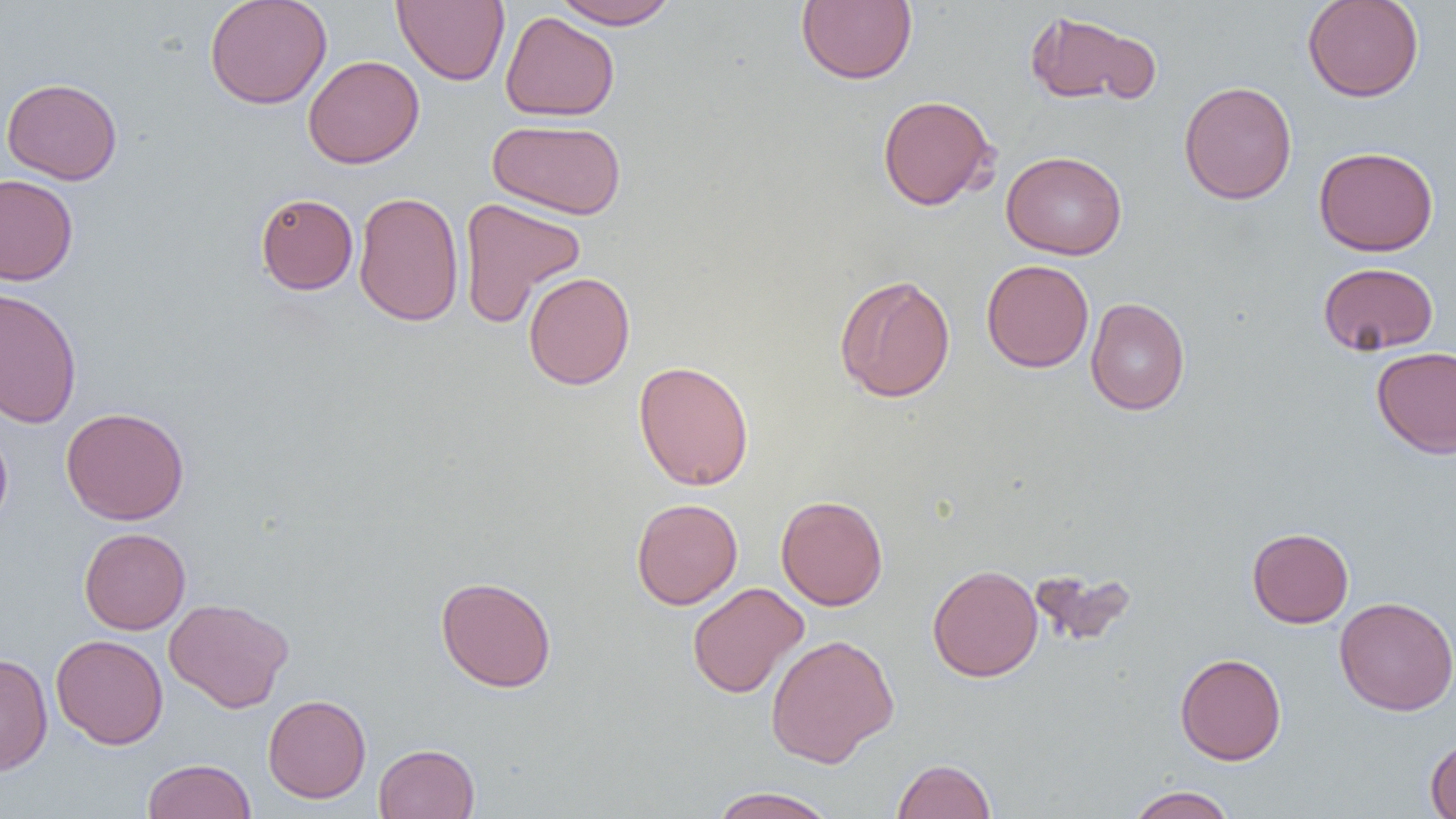

Approximate bounding boxes as (x1, y1, x2, y2) in pixels. Uninfected red blood cell locations: (204, 0, 333, 110), (393, 0, 510, 86), (551, 0, 680, 29), (796, 0, 917, 85), (1302, 0, 1423, 102), (1024, 10, 1160, 106), (500, 11, 619, 122), (303, 55, 424, 169), (1, 77, 123, 184), (1178, 80, 1297, 204), (877, 95, 998, 210), (488, 118, 627, 220), (1313, 146, 1439, 256), (1001, 150, 1127, 260), (0, 173, 79, 285), (353, 190, 464, 327), (255, 193, 359, 295), (459, 197, 586, 326), (981, 259, 1094, 372), (1318, 262, 1439, 355), (523, 271, 635, 389), (834, 273, 956, 403), (0, 287, 83, 428), (1085, 297, 1190, 415), (1371, 345, 1456, 459), (633, 360, 755, 491), (61, 406, 190, 525), (0, 424, 13, 535), (776, 495, 888, 610), (631, 498, 743, 609), (79, 527, 191, 634), (1247, 527, 1354, 628), (927, 564, 1043, 682), (1029, 567, 1137, 648), (435, 576, 557, 692), (686, 582, 809, 699), (1334, 596, 1456, 716), (163, 597, 294, 713), (765, 633, 899, 767), (50, 634, 169, 749), (1175, 652, 1286, 765), (0, 653, 53, 776), (263, 694, 372, 803), (1425, 734, 1456, 819), (373, 743, 480, 819), (142, 758, 256, 819), (891, 758, 997, 819), (1126, 785, 1237, 819), (710, 787, 839, 819). Slide-level diagnosis: negative for blood parasites. Captured at 1000x magnification. Optical microscopy. One field of a larger specimen. Thin blood film. Image is 1456×819 pixels.